Assess this cell for malaria.
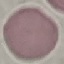

Uninfected.

Summary:
  - Stain: Giemsa
  - Preparation: thin smear
  - Image type: automatically extracted cell patch, resized to 64 × 64 pixels
  - Capture: smartphone camera at the microscope eyepiece